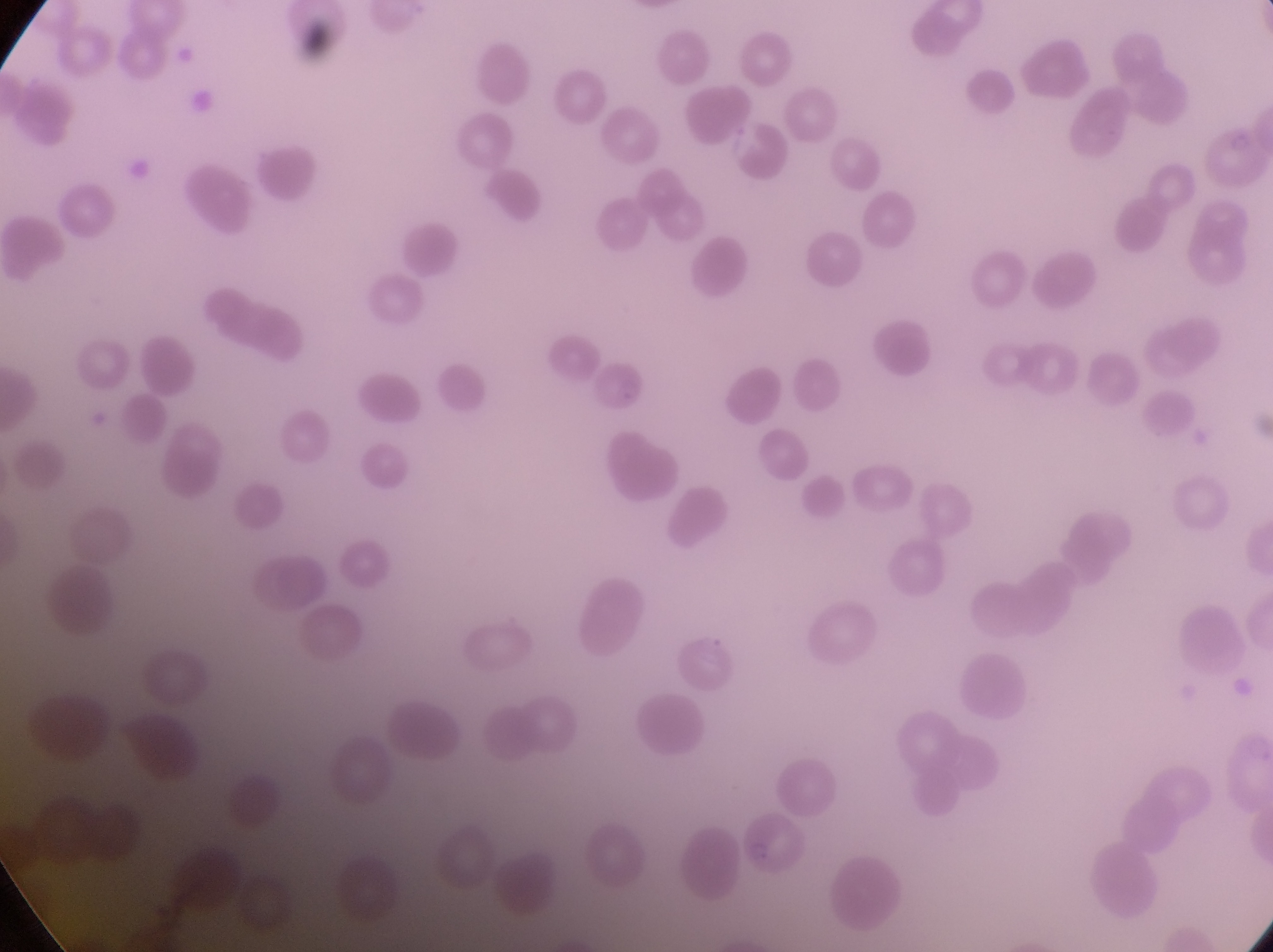

Approximate bounding boxes as {left, top, right, bottom} in pixels.
Summary:
  - Artifact (platelet-like body, stain precipitate, or debris) locations: {127, 148, 162, 187}
  - Preparation: thin blood smear
  - Image size: 1273×952 pixels
  - Capture: smartphone photograph through the eyepiece of an Olympus CX-23 microscope
  - Magnification: 1000x
  - Field of view: single
  - Country: Uganda